Comment on the morphology of the erythrocytes.
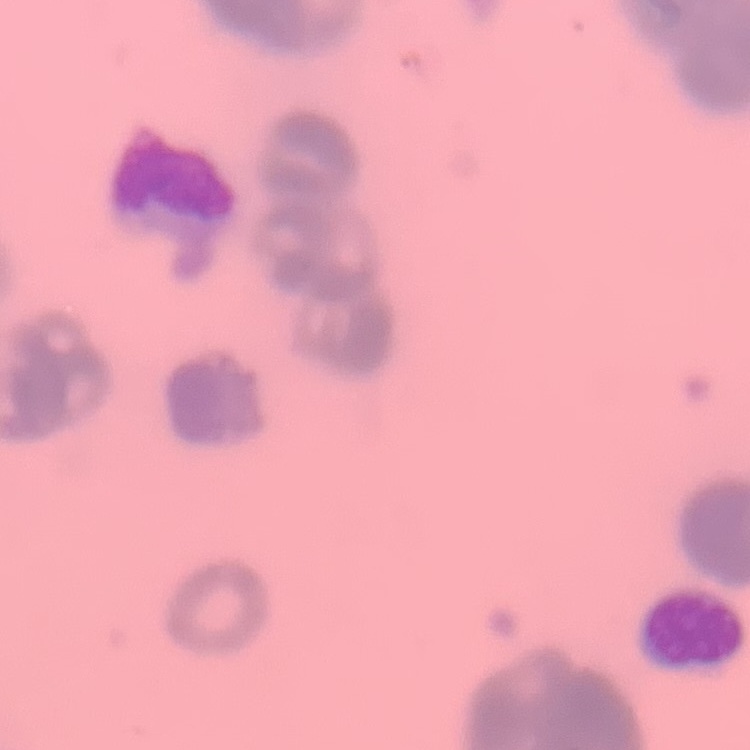

They show rouleaux formation.

preparation = thin peripheral smear
image type = square crop of a larger photomicrograph
stain = Field's or Giemsa